Report the malaria status of this cell.
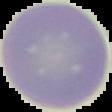
It is uninfected.

Segmented cell region on a black background. From a thin blood smear. Image is 112×112 pixels.